Classify this cell by malaria status.
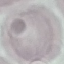
It is uninfected.

capture: smartphone through the microscope eyepiece
image_type: cell patch, automatically extracted from a larger field of view and resized to 64 × 64 pixels
stain: Giemsa
preparation: thin smear